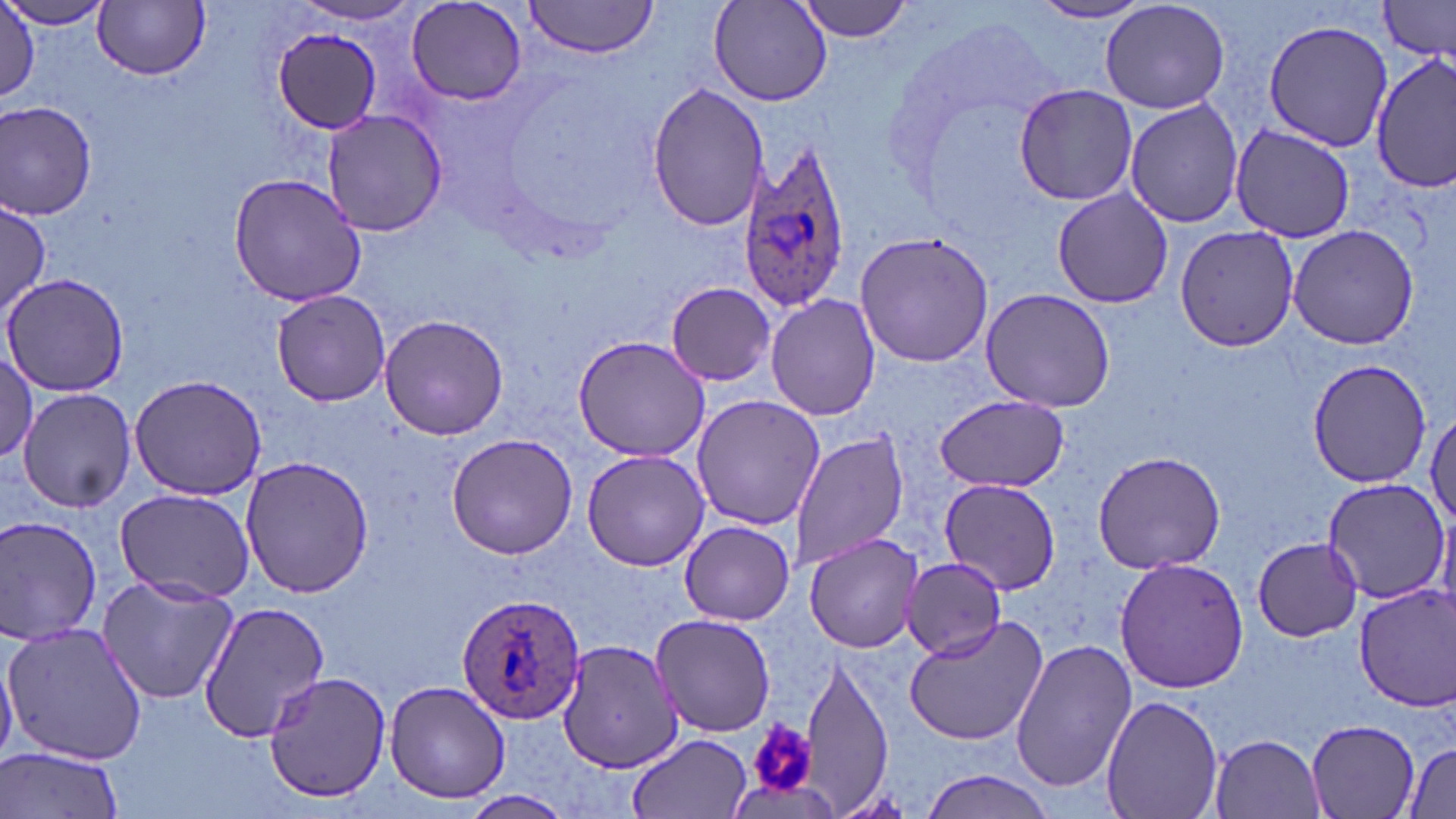
Summary:
  - Coordinate format: approximate bounding boxes as (x1, y1, x2, y2) in pixels
  - Platelet locations: (746, 719, 819, 800)
  - Uninfected red blood cell locations: (0, 0, 112, 30), (523, 0, 662, 58), (797, 0, 916, 42), (1031, 0, 1155, 24), (1100, 0, 1231, 115), (1379, 0, 1455, 61), (708, 1, 833, 108), (94, 2, 211, 80), (406, 2, 528, 108), (291, 3, 426, 27), (1, 8, 39, 104), (1263, 20, 1392, 152), (272, 27, 386, 134), (1372, 53, 1455, 197), (1013, 83, 1141, 207), (646, 84, 768, 233), (1124, 99, 1246, 227), (0, 101, 98, 220), (320, 107, 446, 237), (1229, 124, 1356, 242), (227, 172, 369, 307), (1051, 189, 1173, 309), (0, 199, 50, 320), (1174, 225, 1301, 351), (1287, 226, 1420, 349), (853, 231, 993, 368), (3, 272, 129, 397), (665, 282, 775, 384), (982, 287, 1115, 413), (269, 288, 393, 407), (765, 293, 881, 422), (379, 314, 510, 441), (572, 334, 711, 462), (0, 348, 39, 466), (1304, 358, 1434, 488), (128, 374, 268, 501), (17, 388, 136, 513), (689, 393, 824, 531), (935, 396, 1069, 490), (1428, 404, 1456, 531), (790, 429, 910, 573), (446, 433, 578, 559), (581, 449, 709, 571), (1092, 450, 1225, 573), (240, 455, 375, 599), (937, 477, 1063, 594), (1320, 478, 1453, 603), (115, 487, 256, 604), (0, 516, 104, 644), (679, 521, 796, 625), (804, 533, 925, 654), (1252, 537, 1362, 641), (902, 555, 1007, 660), (1115, 557, 1249, 693), (97, 574, 240, 705), (1354, 585, 1455, 711), (197, 599, 332, 742), (650, 612, 778, 737), (904, 614, 1052, 748), (3, 622, 151, 766), (557, 639, 682, 774), (1011, 640, 1134, 793), (0, 644, 18, 768), (801, 651, 892, 812), (261, 671, 391, 801), (384, 679, 512, 804), (1102, 694, 1224, 819), (1305, 719, 1422, 819), (627, 733, 753, 819), (1209, 733, 1326, 818), (1402, 742, 1455, 818), (1, 745, 125, 819), (921, 769, 1057, 818), (464, 790, 571, 817)
  - Plasmodium ovale-infected red blood cell locations: (735, 146, 852, 308), (456, 592, 588, 724)
  - Slide-level diagnosis: Plasmodium ovale
  - Magnification: 1000x
  - Stain: May-Grünwald-Giemsa
  - Modality: optical microscopy
  - Image size: 1456×819 pixels
  - Field of view: single
  - Preparation: thin blood film